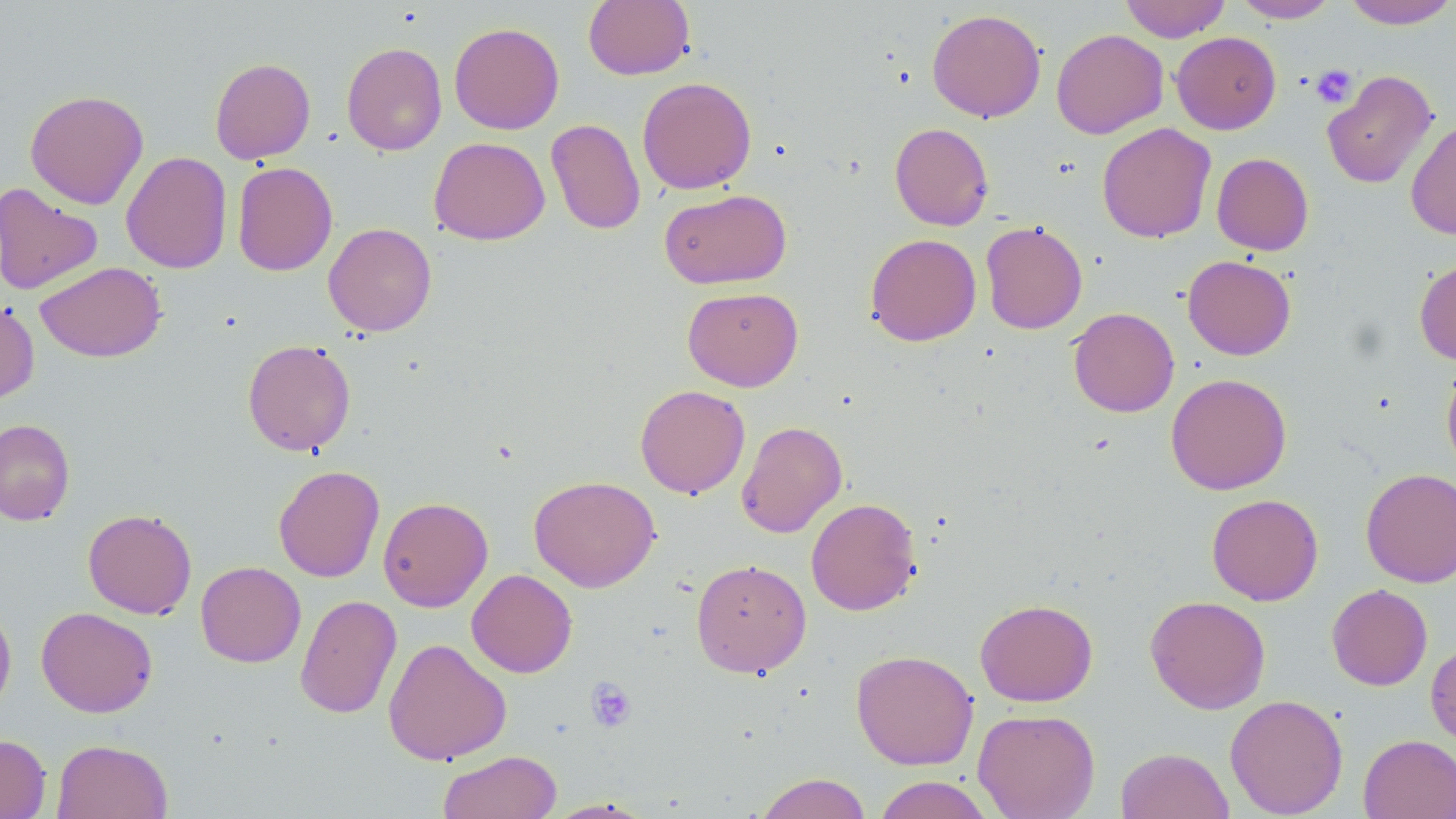
Summary:
  - Coordinate format: approximate bounding boxes as named x1/y1/x2/y2 corners in pixels
  - Uninfected red blood cell locations: (x1=583, y1=0, x2=695, y2=80), (x1=1120, y1=0, x2=1230, y2=42), (x1=1232, y1=0, x2=1339, y2=23), (x1=1342, y1=0, x2=1456, y2=30), (x1=927, y1=8, x2=1046, y2=122), (x1=449, y1=22, x2=564, y2=134), (x1=1051, y1=28, x2=1168, y2=139), (x1=1171, y1=31, x2=1281, y2=134), (x1=341, y1=42, x2=447, y2=156), (x1=210, y1=58, x2=315, y2=163), (x1=1321, y1=69, x2=1437, y2=189), (x1=637, y1=76, x2=757, y2=194), (x1=24, y1=89, x2=149, y2=209), (x1=546, y1=118, x2=646, y2=235), (x1=1406, y1=118, x2=1456, y2=240), (x1=889, y1=123, x2=994, y2=231), (x1=1096, y1=123, x2=1216, y2=243), (x1=429, y1=137, x2=550, y2=245), (x1=120, y1=151, x2=232, y2=274), (x1=1212, y1=152, x2=1314, y2=255), (x1=232, y1=161, x2=337, y2=276), (x1=0, y1=183, x2=103, y2=296), (x1=659, y1=188, x2=792, y2=289), (x1=980, y1=221, x2=1087, y2=334), (x1=323, y1=222, x2=437, y2=336), (x1=865, y1=233, x2=981, y2=346), (x1=1182, y1=255, x2=1296, y2=360), (x1=1414, y1=258, x2=1456, y2=366), (x1=35, y1=261, x2=166, y2=362), (x1=682, y1=287, x2=803, y2=391), (x1=0, y1=299, x2=39, y2=405), (x1=1068, y1=307, x2=1179, y2=417), (x1=242, y1=339, x2=356, y2=456), (x1=1440, y1=358, x2=1456, y2=476), (x1=1165, y1=373, x2=1292, y2=495), (x1=635, y1=384, x2=750, y2=498), (x1=0, y1=419, x2=75, y2=525), (x1=736, y1=420, x2=848, y2=538), (x1=273, y1=465, x2=385, y2=582), (x1=1360, y1=468, x2=1456, y2=588), (x1=529, y1=475, x2=661, y2=592), (x1=1206, y1=493, x2=1323, y2=606), (x1=378, y1=496, x2=493, y2=612), (x1=805, y1=497, x2=922, y2=616), (x1=83, y1=509, x2=197, y2=619), (x1=691, y1=558, x2=812, y2=678), (x1=196, y1=561, x2=305, y2=667), (x1=467, y1=569, x2=577, y2=678), (x1=1326, y1=584, x2=1432, y2=691), (x1=295, y1=594, x2=402, y2=719), (x1=1145, y1=595, x2=1271, y2=714), (x1=975, y1=598, x2=1098, y2=706), (x1=0, y1=602, x2=17, y2=717), (x1=36, y1=607, x2=158, y2=717), (x1=1425, y1=637, x2=1456, y2=747), (x1=383, y1=638, x2=511, y2=765), (x1=851, y1=649, x2=978, y2=770), (x1=1224, y1=694, x2=1348, y2=818), (x1=973, y1=708, x2=1100, y2=819), (x1=0, y1=734, x2=51, y2=819), (x1=1358, y1=734, x2=1456, y2=819), (x1=52, y1=739, x2=172, y2=819), (x1=1116, y1=746, x2=1234, y2=819), (x1=438, y1=750, x2=561, y2=818), (x1=754, y1=772, x2=873, y2=819), (x1=872, y1=775, x2=995, y2=819), (x1=543, y1=798, x2=658, y2=818)
  - Platelet locations: (x1=1310, y1=64, x2=1358, y2=107), (x1=585, y1=677, x2=637, y2=732)
  - Slide-level diagnosis: negative for blood parasites
  - Field of view: one of a larger specimen
  - Image size: 1456×819 pixels
  - Magnification: 1000x
  - Stain: May-Grünwald-Giemsa
  - Preparation: thin blood film
  - Modality: optical microscopy